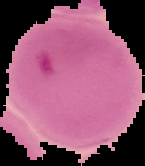

Summary:
  - Preparation: thin blood smear
  - Malaria status: parasitized
  - Image size: 145×166 pixels
  - Image type: segmented cell region with the area outside set to black